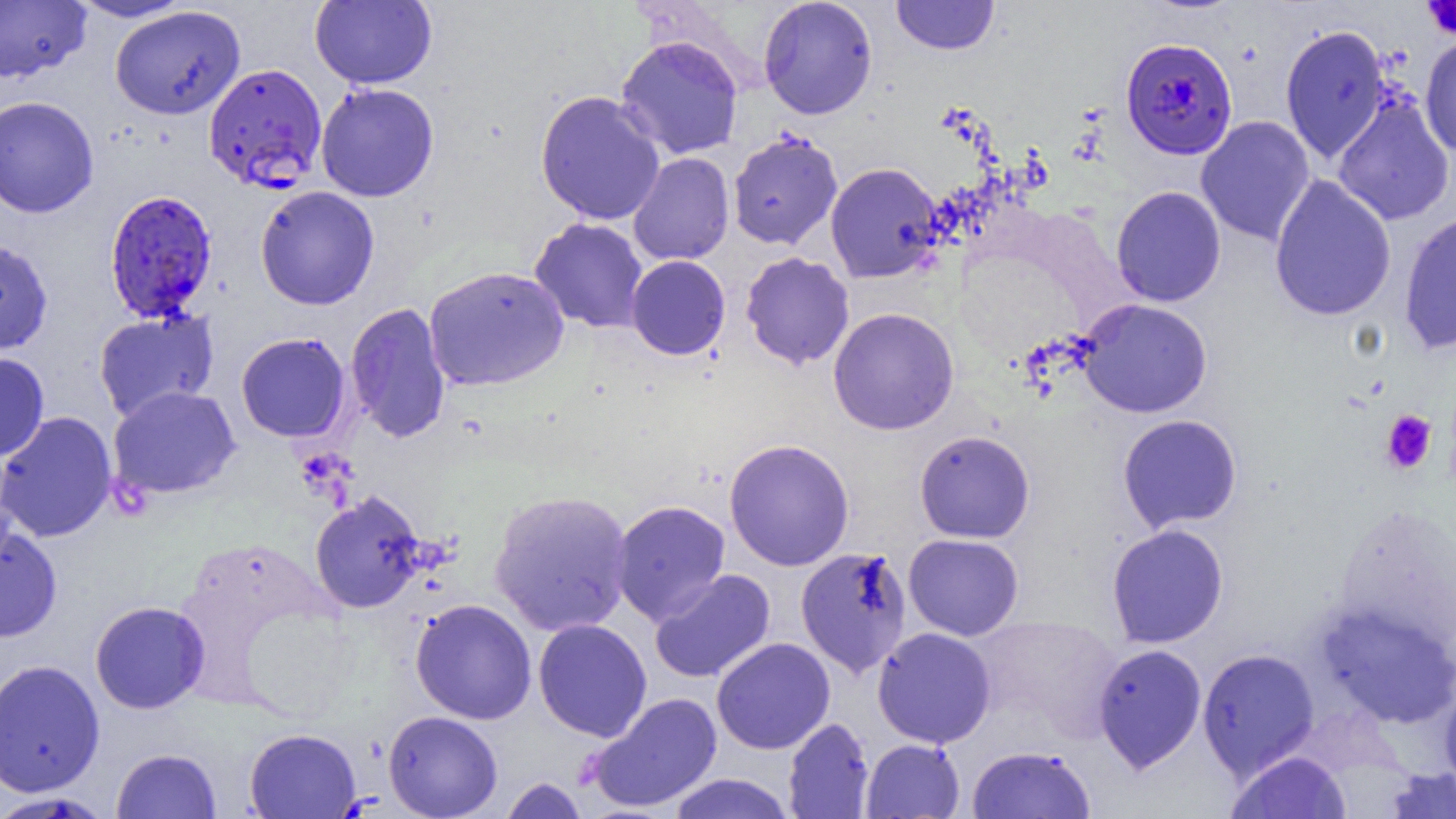
Summary:
  - Coordinate format: approximate bounding boxes as (x1,y1)-(x2,y2) corner pairs in pixels
  - Uninfected red blood cell locations: (68,0)-(196,22), (310,0)-(436,89), (758,0)-(877,119), (891,0)-(999,55), (0,1)-(91,83), (110,5)-(246,120), (1280,25)-(1391,163), (615,35)-(744,159), (1419,35)-(1456,157), (315,82)-(439,202), (535,90)-(666,226), (1333,94)-(1454,226), (0,95)-(100,218), (1195,116)-(1316,246), (728,130)-(843,249), (628,152)-(734,266), (825,162)-(944,283), (1268,175)-(1396,322), (255,185)-(380,310), (1110,185)-(1226,307), (1398,211)-(1456,354), (530,218)-(649,333), (0,237)-(53,356), (740,252)-(855,370), (626,255)-(731,360), (423,265)-(570,392), (1077,298)-(1212,418), (345,302)-(452,443), (828,307)-(960,435), (93,310)-(219,422), (236,332)-(351,442), (0,352)-(50,461), (108,385)-(241,500), (0,411)-(117,542), (1117,413)-(1242,533), (914,430)-(1035,543), (724,438)-(855,571), (489,489)-(633,637), (309,490)-(428,613), (610,500)-(731,625), (1106,523)-(1229,649), (0,524)-(62,642), (903,534)-(1024,640), (796,546)-(913,679), (649,569)-(776,684), (410,598)-(537,724), (89,601)-(210,714), (1316,602)-(1456,728), (974,617)-(1125,742), (533,618)-(652,741), (872,626)-(997,748), (711,637)-(835,755), (1093,643)-(1207,773), (1197,648)-(1321,780), (0,658)-(105,797), (1438,679)-(1456,798), (586,692)-(722,813), (383,710)-(503,819), (783,717)-(874,818), (244,728)-(361,818), (861,738)-(965,818), (966,745)-(1096,818), (111,748)-(221,819), (1224,750)-(1352,819), (1382,767)-(1456,818), (667,773)-(795,819), (499,776)-(589,819), (0,792)-(112,819)
  - Platelet locations: (1421,0)-(1456,43), (1380,410)-(1437,475)
  - Plasmodium falciparum-infected red blood cell locations: (1121,37)-(1237,159), (203,63)-(328,191), (104,189)-(218,323)
  - Slide-level diagnosis: Plasmodium falciparum
  - Magnification: 1000x
  - Modality: optical microscopy
  - Field of view: one of a larger specimen
  - Preparation: thin blood film
  - Image size: 1456×819 pixels